Name the parasite shown.
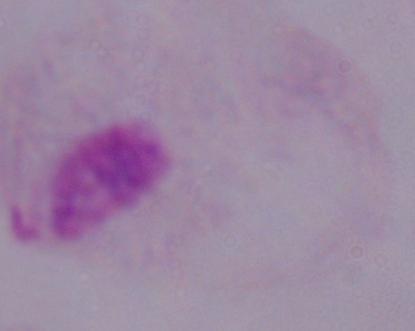
A trichomonad.

Summary:
  - Magnification: 1000x
  - Modality: micrograph